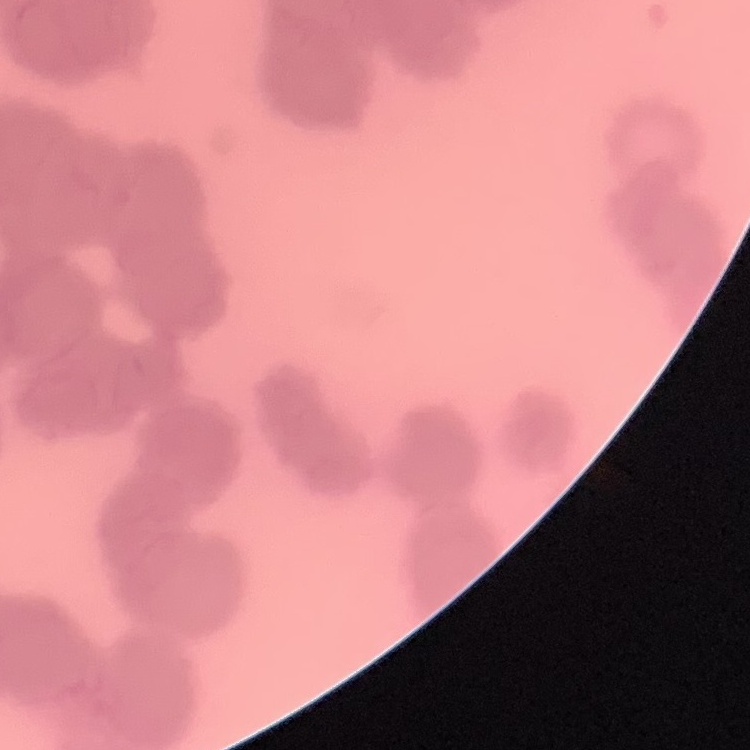

erythrocyte morphology = rouleaux formation
stain = Field's or Giemsa
preparation = thin blood smear
image type = square crop of a larger photomicrograph